Identify the parasite.
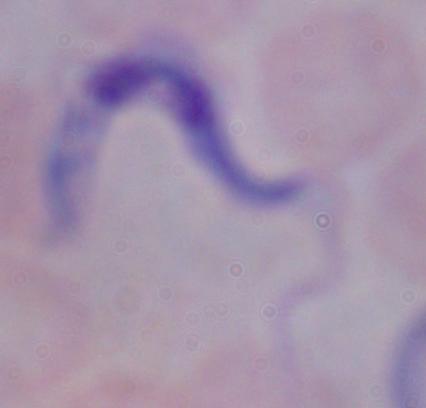

A trypanosome.

Photomicrograph. Captured at 1000x magnification.